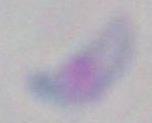
{
  "identification": "Toxoplasma gondii",
  "magnification": "1000x",
  "modality": "micrograph"
}